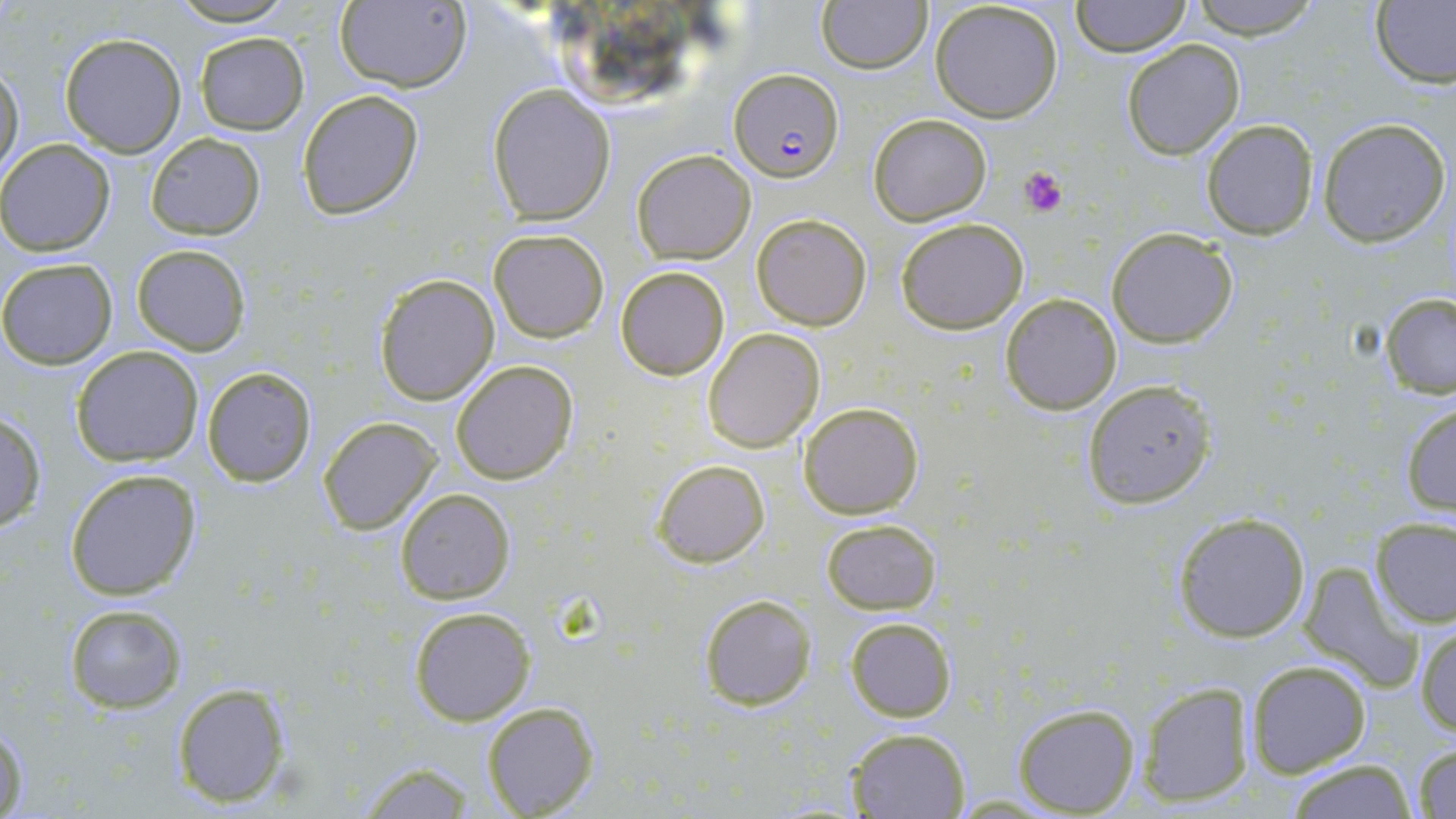

slide-level diagnosis = Plasmodium falciparum
field of view = single
uninfected red blood cell locations = approximate bounding boxes as (x1, y1, x2, y2) in pixels: (166, 0, 300, 25), (333, 0, 471, 92), (1184, 0, 1327, 40), (816, 1, 931, 74), (929, 1, 1065, 123), (1071, 1, 1193, 55), (1372, 1, 1456, 89), (58, 32, 187, 156), (194, 32, 309, 135), (1122, 39, 1246, 160), (1, 63, 24, 177), (488, 84, 616, 224), (296, 88, 423, 219), (868, 113, 992, 225), (1201, 118, 1318, 240), (1318, 118, 1451, 247), (146, 133, 265, 240), (0, 138, 115, 256), (631, 148, 756, 264), (750, 212, 873, 331), (897, 217, 1029, 334), (1106, 227, 1238, 348), (489, 228, 609, 342), (130, 244, 251, 355), (1, 258, 117, 369), (615, 265, 730, 380), (374, 273, 499, 406), (999, 293, 1122, 413), (1380, 293, 1456, 398), (702, 328, 826, 453), (71, 346, 203, 465), (450, 359, 579, 485), (201, 366, 318, 487), (1082, 380, 1218, 508), (798, 401, 923, 519), (1401, 403, 1455, 516), (0, 410, 46, 534), (318, 418, 441, 534), (653, 459, 770, 567), (64, 469, 200, 600), (396, 489, 516, 604), (1171, 511, 1310, 642), (1371, 516, 1456, 628), (820, 517, 941, 615), (1300, 565, 1421, 690), (697, 594, 817, 712), (65, 604, 186, 712), (408, 605, 537, 726), (845, 617, 956, 722), (1416, 623, 1456, 737), (1245, 661, 1371, 778), (172, 682, 292, 807), (1138, 682, 1252, 806), (481, 701, 601, 817), (1013, 703, 1139, 815), (1, 716, 29, 819), (845, 727, 970, 818), (1412, 744, 1456, 817), (1286, 760, 1415, 819), (347, 761, 483, 818)
platelet locations = approximate bounding boxes as (x1, y1, x2, y2) in pixels: (1020, 167, 1067, 216)
stain = May-Grünwald-Giemsa
Plasmodium falciparum-infected red blood cell locations = approximate bounding boxes as (x1, y1, x2, y2) in pixels: (728, 70, 842, 184)
image size = 1456×819 pixels
magnification = 1000x
preparation = thin blood film
modality = light microscopy